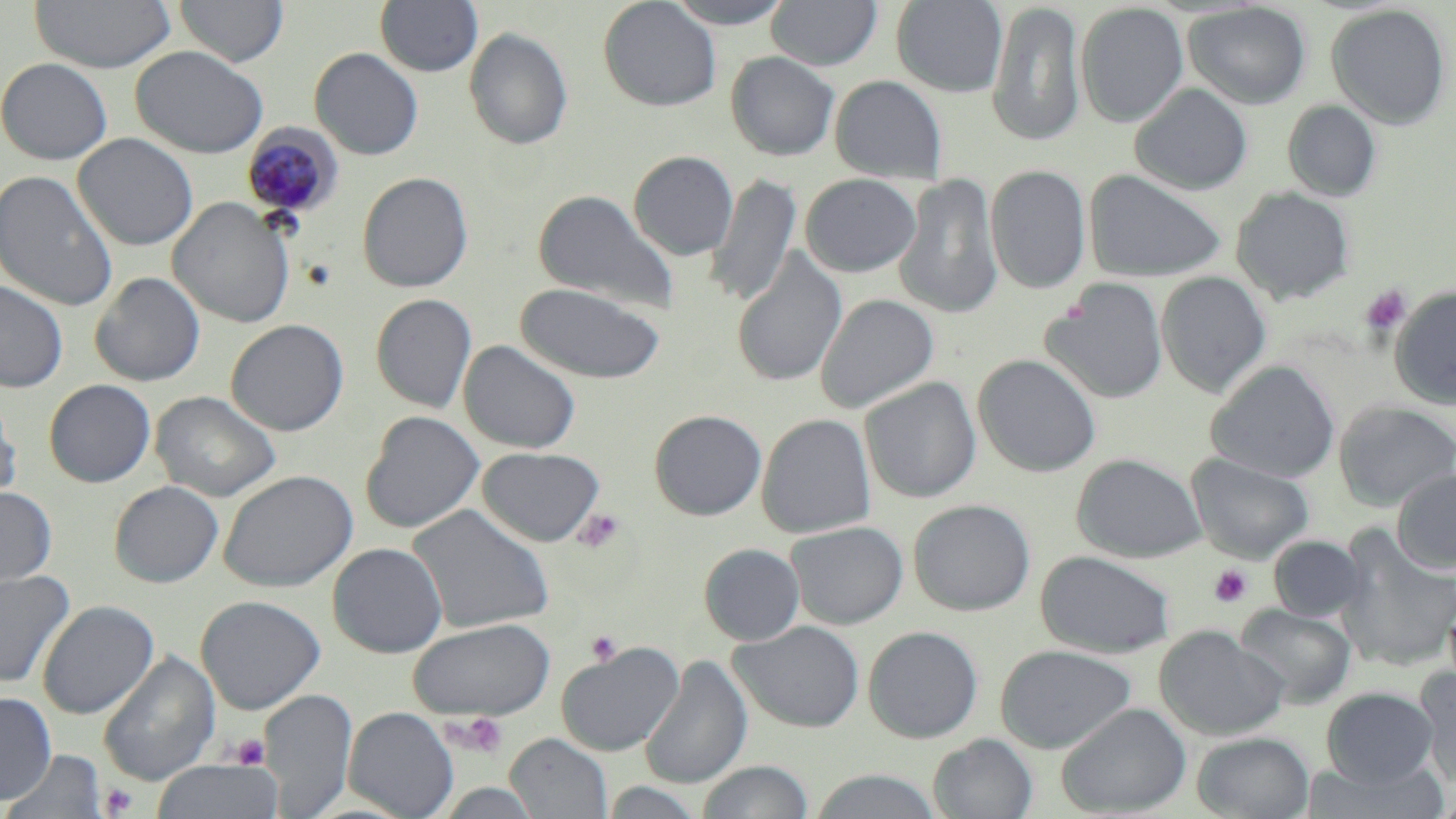
slide-level diagnosis = Plasmodium malariae
platelet locations = approximate bounding boxes as named x1/y1/x2/y2 corners in pixels: (x1=1359, y1=285, x2=1411, y2=335), (x1=574, y1=509, x2=626, y2=553), (x1=1209, y1=564, x2=1253, y2=608), (x1=586, y1=630, x2=622, y2=666), (x1=443, y1=713, x2=509, y2=759), (x1=232, y1=734, x2=270, y2=769), (x1=99, y1=783, x2=138, y2=817)
preparation = thin blood film
uninfected red blood cell locations = approximate bounding boxes as named x1/y1/x2/y2 corners in pixels: (x1=29, y1=0, x2=176, y2=73), (x1=175, y1=0, x2=288, y2=66), (x1=375, y1=0, x2=482, y2=77), (x1=598, y1=0, x2=722, y2=111), (x1=663, y1=0, x2=795, y2=28), (x1=766, y1=0, x2=882, y2=70), (x1=891, y1=0, x2=1008, y2=97), (x1=986, y1=2, x2=1086, y2=147), (x1=1075, y1=2, x2=1188, y2=128), (x1=1183, y1=2, x2=1312, y2=110), (x1=1325, y1=3, x2=1452, y2=130), (x1=464, y1=27, x2=574, y2=151), (x1=131, y1=45, x2=268, y2=158), (x1=310, y1=47, x2=424, y2=160), (x1=725, y1=52, x2=840, y2=160), (x1=0, y1=57, x2=113, y2=165), (x1=830, y1=75, x2=947, y2=184), (x1=1130, y1=83, x2=1253, y2=196), (x1=1282, y1=100, x2=1381, y2=201), (x1=73, y1=133, x2=198, y2=251), (x1=629, y1=150, x2=739, y2=260), (x1=986, y1=165, x2=1091, y2=294), (x1=1083, y1=168, x2=1227, y2=283), (x1=0, y1=170, x2=119, y2=313), (x1=357, y1=171, x2=473, y2=293), (x1=707, y1=173, x2=801, y2=307), (x1=800, y1=173, x2=922, y2=277), (x1=895, y1=173, x2=1004, y2=320), (x1=1231, y1=187, x2=1354, y2=305), (x1=532, y1=188, x2=679, y2=314), (x1=168, y1=197, x2=294, y2=328), (x1=731, y1=247, x2=848, y2=387), (x1=1155, y1=271, x2=1271, y2=397), (x1=90, y1=272, x2=205, y2=387), (x1=1041, y1=277, x2=1169, y2=405), (x1=0, y1=280, x2=68, y2=392), (x1=515, y1=282, x2=666, y2=384), (x1=1389, y1=285, x2=1456, y2=410), (x1=370, y1=293, x2=477, y2=413), (x1=815, y1=293, x2=939, y2=414), (x1=226, y1=318, x2=348, y2=436), (x1=458, y1=339, x2=582, y2=454), (x1=973, y1=354, x2=1101, y2=477), (x1=1205, y1=360, x2=1340, y2=483), (x1=860, y1=376, x2=981, y2=503), (x1=44, y1=379, x2=156, y2=487), (x1=150, y1=390, x2=281, y2=502), (x1=0, y1=392, x2=22, y2=508), (x1=1334, y1=400, x2=1456, y2=511), (x1=649, y1=409, x2=767, y2=520), (x1=360, y1=410, x2=485, y2=534), (x1=756, y1=413, x2=876, y2=539), (x1=476, y1=446, x2=605, y2=546), (x1=1072, y1=453, x2=1206, y2=563), (x1=1186, y1=454, x2=1314, y2=563), (x1=218, y1=469, x2=357, y2=592), (x1=1392, y1=469, x2=1456, y2=574), (x1=109, y1=480, x2=224, y2=588), (x1=0, y1=485, x2=57, y2=591), (x1=908, y1=498, x2=1035, y2=616), (x1=407, y1=504, x2=555, y2=634), (x1=785, y1=520, x2=908, y2=630), (x1=1335, y1=525, x2=1456, y2=672), (x1=1269, y1=535, x2=1365, y2=622), (x1=328, y1=542, x2=448, y2=658), (x1=699, y1=543, x2=805, y2=645), (x1=1035, y1=550, x2=1176, y2=658), (x1=0, y1=569, x2=75, y2=689), (x1=195, y1=595, x2=325, y2=715), (x1=37, y1=600, x2=158, y2=719), (x1=1236, y1=604, x2=1356, y2=709), (x1=407, y1=617, x2=556, y2=720), (x1=730, y1=621, x2=865, y2=733), (x1=1155, y1=625, x2=1288, y2=741), (x1=863, y1=626, x2=983, y2=743), (x1=558, y1=642, x2=684, y2=755), (x1=995, y1=644, x2=1137, y2=752), (x1=98, y1=650, x2=220, y2=785), (x1=639, y1=654, x2=753, y2=789), (x1=1414, y1=666, x2=1456, y2=788), (x1=1321, y1=687, x2=1438, y2=786), (x1=260, y1=689, x2=357, y2=817), (x1=0, y1=691, x2=56, y2=804), (x1=1056, y1=702, x2=1192, y2=817), (x1=343, y1=706, x2=459, y2=819), (x1=1192, y1=731, x2=1315, y2=819), (x1=505, y1=733, x2=612, y2=819), (x1=928, y1=734, x2=1039, y2=819), (x1=3, y1=749, x2=107, y2=818), (x1=150, y1=759, x2=283, y2=819), (x1=697, y1=759, x2=814, y2=819), (x1=1298, y1=759, x2=1452, y2=818), (x1=807, y1=769, x2=946, y2=819), (x1=600, y1=781, x2=708, y2=819), (x1=434, y1=782, x2=543, y2=819)
Plasmodium malariae-infected red blood cell locations = approximate bounding boxes as named x1/y1/x2/y2 corners in pixels: (x1=242, y1=123, x2=344, y2=222)
image size = 1456×819 pixels
stain = May-Grünwald-Giemsa
magnification = 1000x
field of view = single
modality = light microscopy